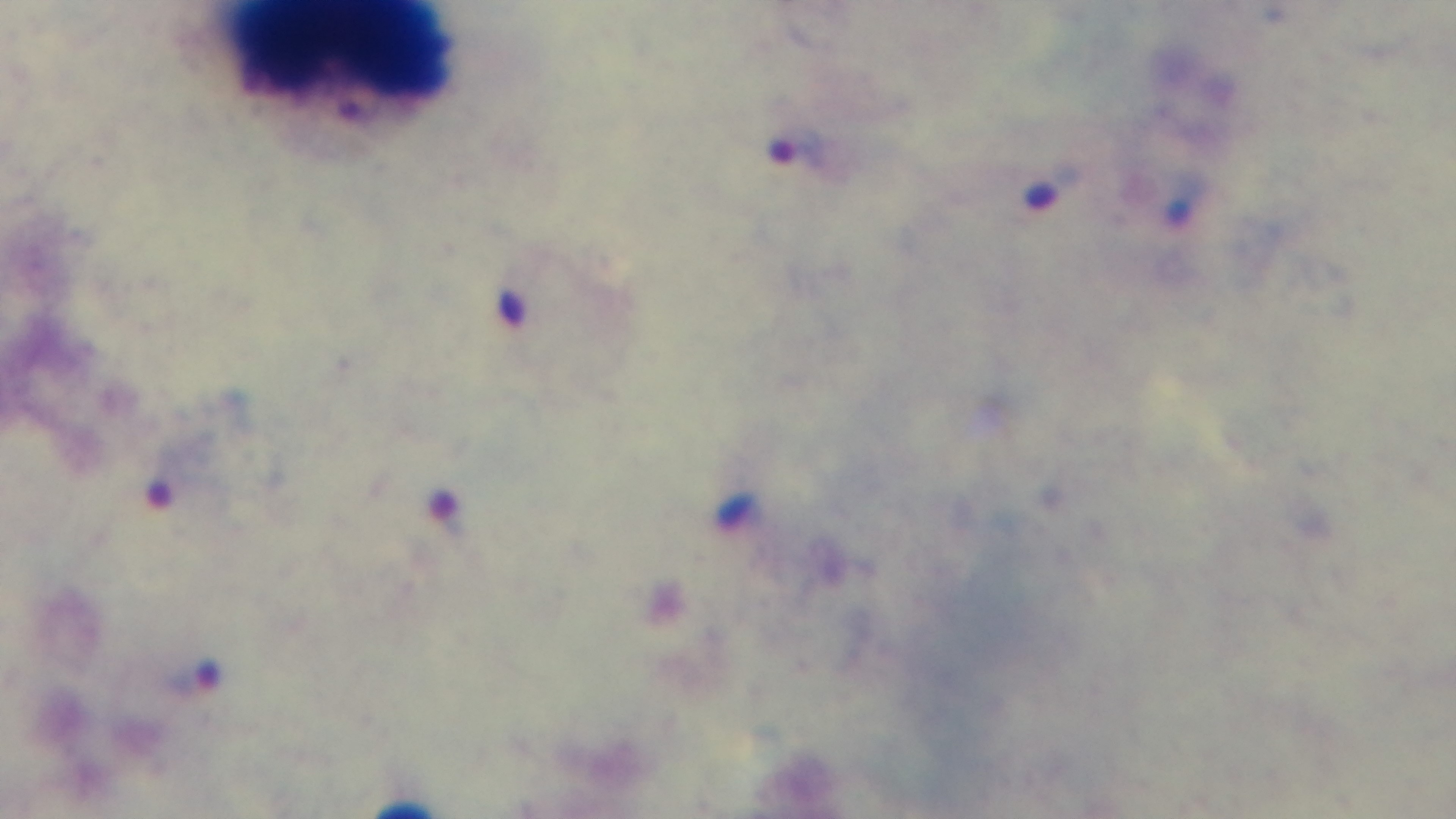

Giemsa-stained. Photomicrograph. One field from the slide. Malaria status: positive. 100x oil-immersion objective. Preparation: thick. Captured with a mounted 4K digital camera.